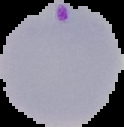

Summary:
  - Preparation: thin blood film
  - Result: malaria parasites detected
  - Image size: 124×127 pixels
  - Image type: cell region segmented out of the field of view; surrounding area masked to black